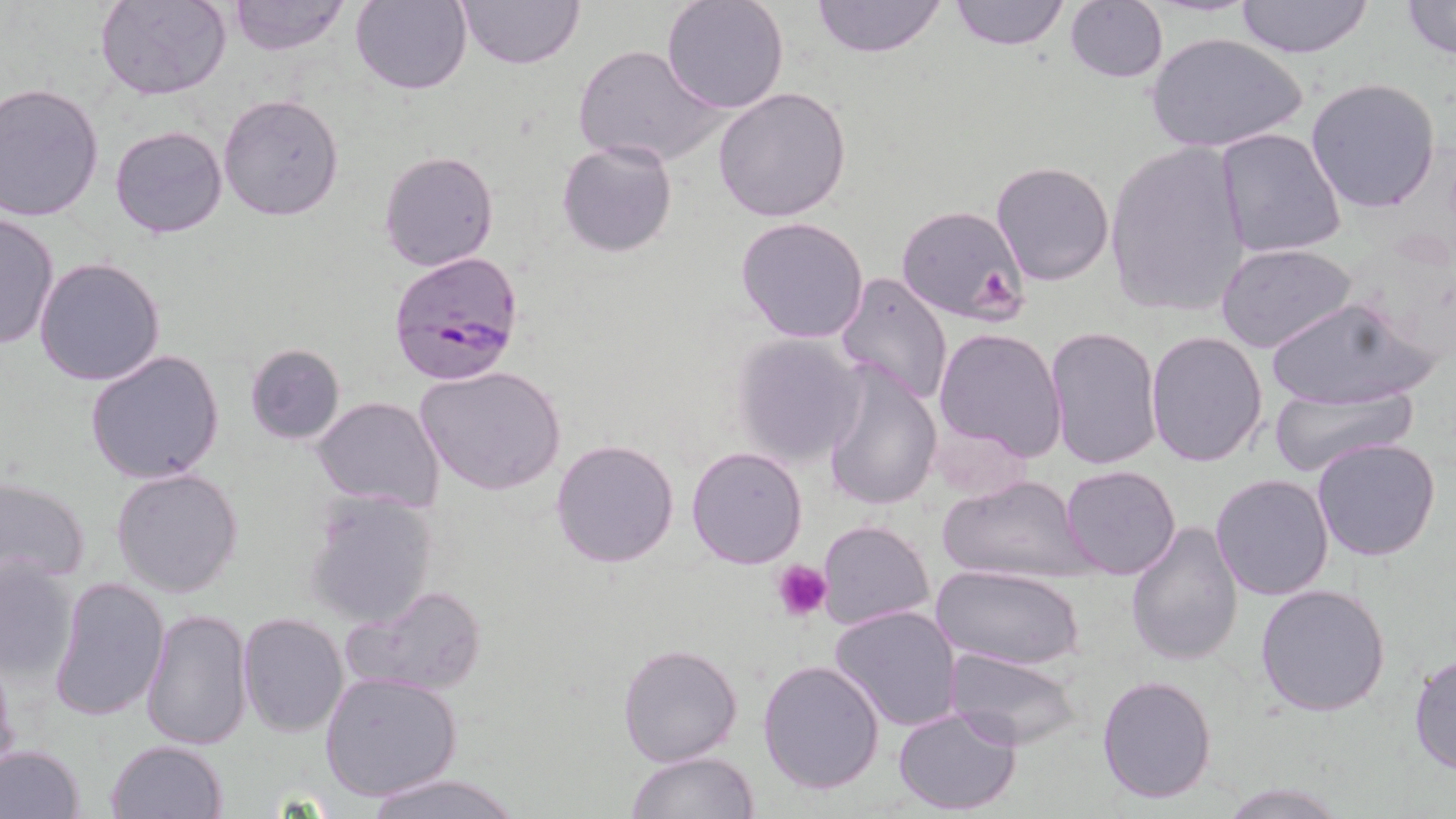

slide-level diagnosis = Plasmodium falciparum
preparation = thin blood film
magnification = 1000x
stain = May-Grünwald-Giemsa
uninfected red blood cell locations = approximate bounding boxes as (x1, y1, x2, y2) in pixels: (97, 0, 229, 101), (350, 0, 472, 96), (454, 0, 586, 70), (810, 0, 948, 58), (949, 0, 1070, 50), (1233, 0, 1374, 58), (227, 1, 348, 55), (660, 1, 789, 114), (1064, 1, 1168, 84), (1401, 1, 1456, 61), (1146, 33, 1307, 155), (573, 44, 725, 168), (1306, 77, 1442, 214), (0, 83, 105, 222), (713, 87, 852, 222), (218, 95, 346, 221), (109, 125, 229, 239), (1214, 128, 1347, 260), (556, 139, 678, 258), (1104, 140, 1251, 318), (378, 150, 498, 272), (988, 160, 1115, 286), (895, 205, 1029, 325), (0, 210, 58, 351), (735, 215, 870, 344), (1216, 242, 1358, 354), (34, 258, 166, 387), (835, 272, 953, 405), (1262, 297, 1433, 410), (1046, 324, 1163, 470), (933, 327, 1069, 463), (1145, 331, 1269, 467), (731, 333, 865, 465), (244, 343, 345, 445), (85, 349, 225, 484), (820, 361, 942, 512), (415, 365, 567, 496), (1268, 382, 1421, 477), (311, 395, 445, 513), (1311, 437, 1443, 561), (550, 439, 680, 569), (686, 445, 809, 569), (1060, 465, 1181, 581), (111, 467, 243, 599), (935, 471, 1097, 587), (1210, 474, 1334, 601), (1, 476, 92, 586), (302, 493, 440, 630), (815, 519, 934, 631), (1124, 519, 1244, 665), (0, 555, 79, 684), (933, 565, 1083, 673), (47, 575, 172, 724), (346, 584, 489, 699), (1255, 585, 1392, 717), (830, 604, 963, 731), (141, 608, 253, 751), (238, 611, 348, 736), (616, 642, 744, 767), (943, 647, 1083, 752), (0, 651, 19, 783), (1410, 653, 1456, 775), (758, 658, 887, 795), (320, 671, 463, 802), (1097, 674, 1218, 804), (893, 707, 1023, 815), (106, 740, 228, 819), (1, 745, 85, 818), (626, 752, 758, 819), (360, 774, 526, 819), (1220, 780, 1344, 817)
Plasmodium falciparum-infected red blood cell locations = approximate bounding boxes as (x1, y1, x2, y2) in pixels: (389, 252, 524, 386)
platelet locations = approximate bounding boxes as (x1, y1, x2, y2) in pixels: (772, 559, 832, 620)
modality = optical microscopy
field of view = single
image size = 1456×819 pixels